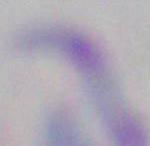

{
  "modality": "micrograph",
  "identification": "Toxoplasma gondii",
  "magnification": "1000x"
}